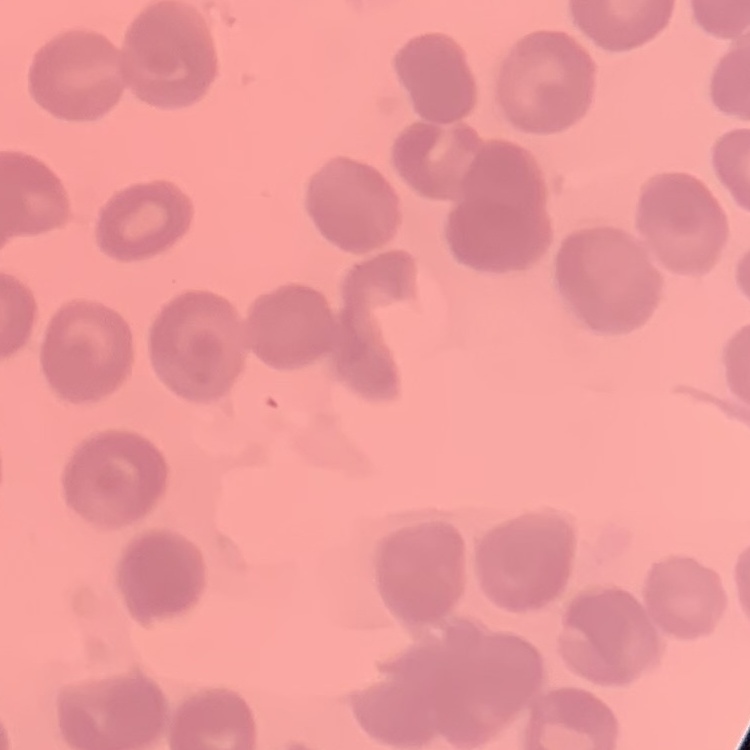
erythrocyte morphology = no rouleaux formation
stain = Field's or Giemsa
image type = square crop of a larger photomicrograph
preparation = thin blood smear